Assess the morphology of the erythrocytes.
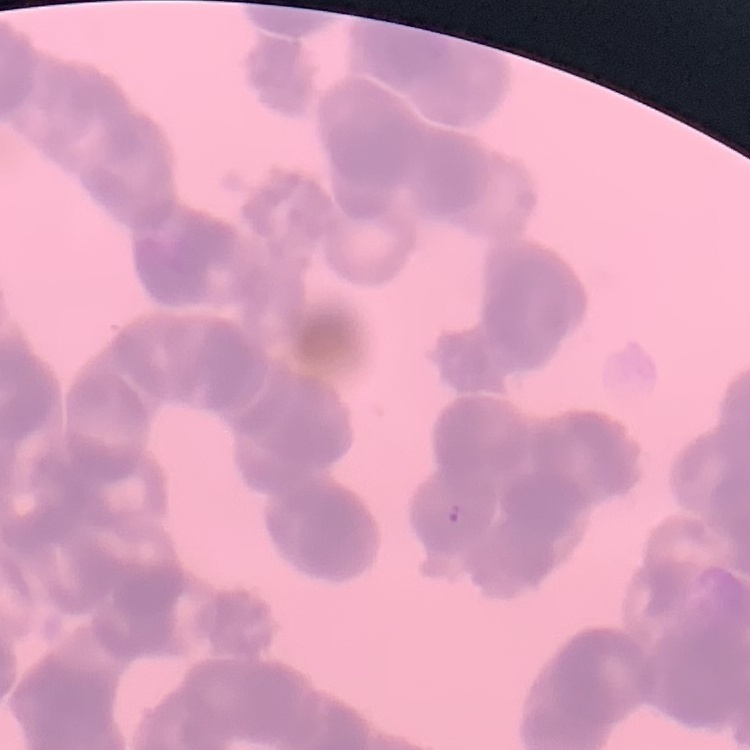
Rouleaux formation.

image_type: one tile cut from a larger photomicrograph
stain: Field's or Giemsa
preparation: thin peripheral smear